Outline each Plasmodium ovale-infected red blood cell.
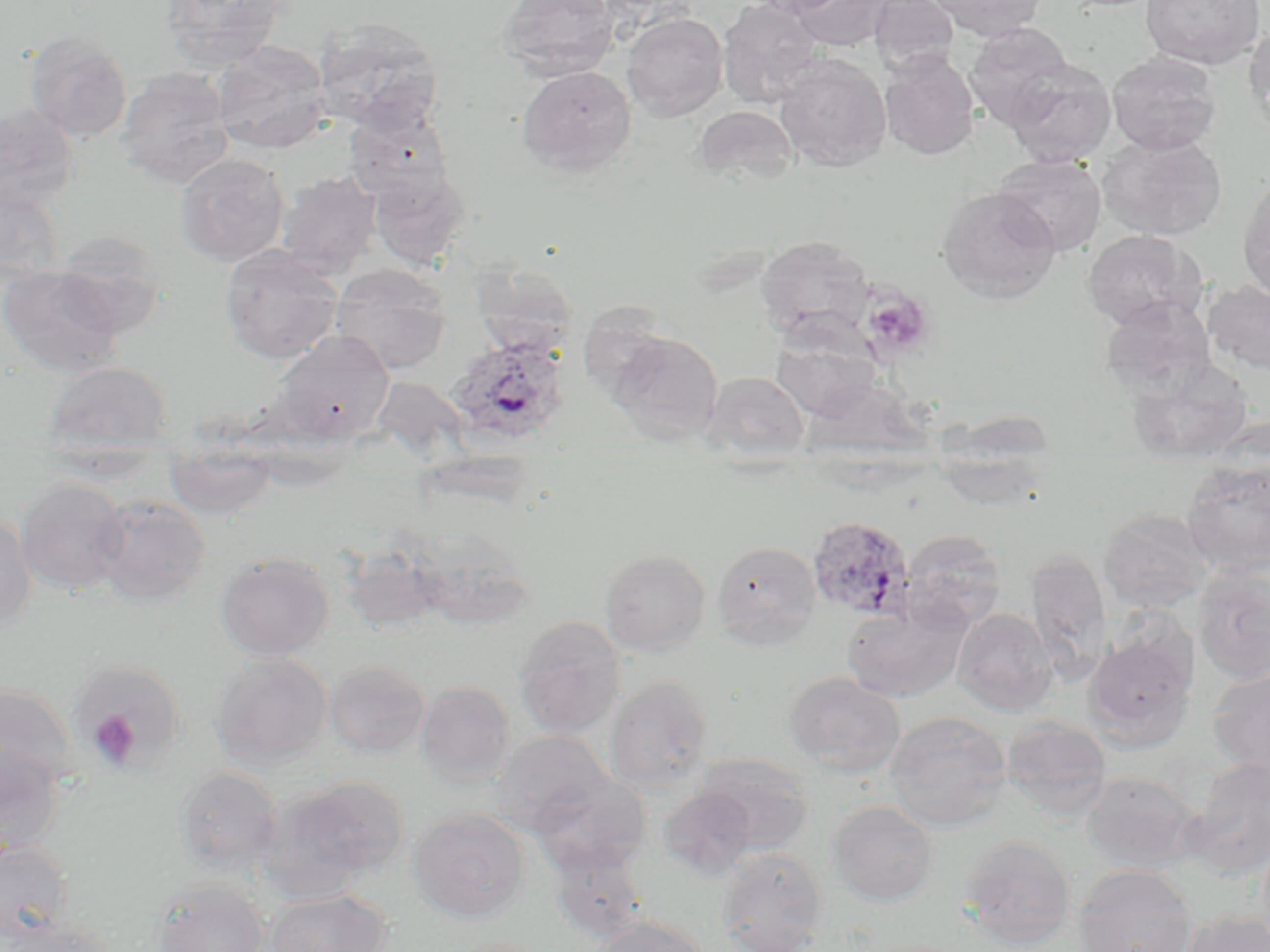

Approximate bounding boxes as named x1/y1/x2/y2 corners in pixels.
Plasmodium ovale-infected red blood cells: (x1=446, y1=335, x2=572, y2=446), (x1=805, y1=515, x2=916, y2=623).

Summary:
  - Platelet locations: (x1=862, y1=288, x2=934, y2=360), (x1=88, y1=710, x2=141, y2=769)
  - Uninfected red blood cell locations: (x1=159, y1=0, x2=291, y2=73), (x1=498, y1=0, x2=621, y2=81), (x1=717, y1=0, x2=824, y2=108), (x1=750, y1=0, x2=851, y2=17), (x1=790, y1=0, x2=894, y2=52), (x1=869, y1=0, x2=959, y2=75), (x1=928, y1=0, x2=1048, y2=41), (x1=1141, y1=0, x2=1265, y2=70), (x1=622, y1=12, x2=728, y2=121), (x1=313, y1=18, x2=444, y2=132), (x1=1245, y1=20, x2=1270, y2=129), (x1=964, y1=22, x2=1073, y2=128), (x1=24, y1=30, x2=132, y2=141), (x1=213, y1=41, x2=333, y2=154), (x1=880, y1=51, x2=979, y2=159), (x1=1107, y1=51, x2=1221, y2=155), (x1=774, y1=54, x2=892, y2=173), (x1=1004, y1=58, x2=1117, y2=167), (x1=517, y1=65, x2=637, y2=177), (x1=117, y1=66, x2=236, y2=189), (x1=0, y1=102, x2=78, y2=211), (x1=343, y1=104, x2=456, y2=207), (x1=693, y1=105, x2=798, y2=188), (x1=1096, y1=132, x2=1227, y2=241), (x1=175, y1=153, x2=289, y2=265), (x1=993, y1=154, x2=1107, y2=256), (x1=368, y1=166, x2=471, y2=269), (x1=276, y1=171, x2=383, y2=278), (x1=1238, y1=173, x2=1270, y2=304), (x1=0, y1=183, x2=64, y2=286), (x1=937, y1=186, x2=1061, y2=303), (x1=50, y1=230, x2=166, y2=338), (x1=1082, y1=230, x2=1203, y2=329), (x1=755, y1=235, x2=877, y2=343), (x1=219, y1=244, x2=343, y2=363), (x1=469, y1=259, x2=582, y2=356), (x1=0, y1=264, x2=129, y2=378), (x1=330, y1=264, x2=452, y2=374), (x1=1204, y1=280, x2=1270, y2=374), (x1=1098, y1=296, x2=1216, y2=399), (x1=605, y1=329, x2=724, y2=444), (x1=273, y1=331, x2=395, y2=445), (x1=771, y1=333, x2=884, y2=421), (x1=1125, y1=359, x2=1255, y2=464), (x1=43, y1=361, x2=174, y2=458), (x1=702, y1=371, x2=810, y2=463), (x1=166, y1=441, x2=276, y2=518), (x1=931, y1=446, x2=1053, y2=510), (x1=1181, y1=459, x2=1270, y2=578), (x1=15, y1=478, x2=131, y2=595), (x1=92, y1=496, x2=211, y2=608), (x1=1098, y1=508, x2=1214, y2=614), (x1=0, y1=510, x2=38, y2=634), (x1=403, y1=527, x2=537, y2=631), (x1=899, y1=529, x2=1008, y2=633), (x1=712, y1=540, x2=822, y2=649), (x1=339, y1=545, x2=445, y2=635), (x1=599, y1=548, x2=710, y2=656), (x1=1026, y1=550, x2=1113, y2=686), (x1=214, y1=552, x2=334, y2=661), (x1=1192, y1=564, x2=1270, y2=685), (x1=842, y1=602, x2=968, y2=703), (x1=953, y1=608, x2=1058, y2=715), (x1=513, y1=616, x2=627, y2=738), (x1=1082, y1=632, x2=1197, y2=752), (x1=211, y1=653, x2=333, y2=766), (x1=324, y1=660, x2=431, y2=759), (x1=1206, y1=667, x2=1270, y2=779), (x1=783, y1=671, x2=907, y2=777), (x1=604, y1=675, x2=714, y2=791), (x1=415, y1=681, x2=516, y2=787), (x1=0, y1=682, x2=81, y2=795), (x1=884, y1=710, x2=1012, y2=832), (x1=1001, y1=716, x2=1112, y2=821), (x1=493, y1=730, x2=615, y2=836), (x1=0, y1=742, x2=66, y2=856), (x1=692, y1=754, x2=814, y2=854), (x1=1181, y1=758, x2=1270, y2=879), (x1=174, y1=766, x2=284, y2=876), (x1=528, y1=770, x2=652, y2=875), (x1=1081, y1=771, x2=1198, y2=874), (x1=275, y1=775, x2=411, y2=886), (x1=658, y1=786, x2=759, y2=879), (x1=827, y1=800, x2=939, y2=907), (x1=408, y1=807, x2=531, y2=922), (x1=957, y1=835, x2=1077, y2=950), (x1=543, y1=836, x2=651, y2=945), (x1=0, y1=839, x2=74, y2=945), (x1=717, y1=847, x2=827, y2=952), (x1=1074, y1=864, x2=1198, y2=952), (x1=150, y1=878, x2=269, y2=952), (x1=265, y1=888, x2=393, y2=951), (x1=1180, y1=910, x2=1270, y2=952), (x1=587, y1=916, x2=712, y2=952), (x1=5, y1=917, x2=118, y2=952), (x1=446, y1=937, x2=555, y2=952)
  - Slide-level diagnosis: Plasmodium ovale
  - Magnification: 1000x
  - Image size: 1270×952 pixels
  - Modality: optical microscopy
  - Stain: May-Grünwald-Giemsa
  - Preparation: thin blood film
  - Field of view: single